Identify the parasite.
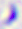
This is Toxoplasma gondii.

magnification: 400x
modality: photomicrograph